Assess this cell for malaria.
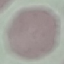
It is uninfected.

Thin blood smear. Cell patch, automatically extracted from a larger field of view and resized to 64 × 64 pixels. Acquired by smartphone through the microscope eyepiece. Giemsa-stained preparation.